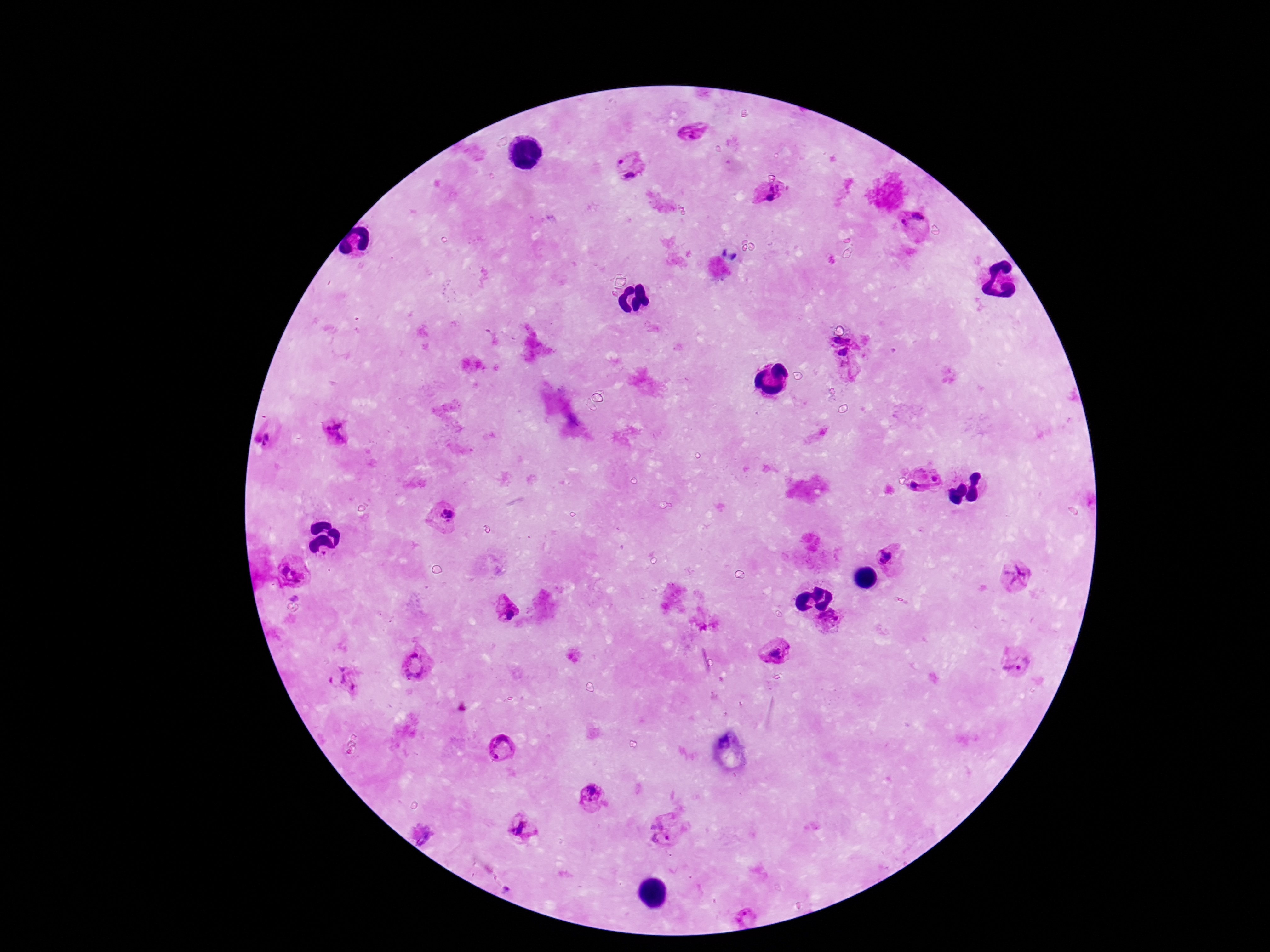 Approximate object centers, in pixels from the top-left corner. Plasmodium parasite locations: (x=693, y=132), (x=623, y=157), (x=631, y=176), (x=777, y=196), (x=912, y=223), (x=838, y=340), (x=845, y=355), (x=334, y=434), (x=268, y=440), (x=935, y=478), (x=917, y=487), (x=446, y=514), (x=888, y=556), (x=291, y=571), (x=1014, y=574), (x=506, y=607), (x=831, y=623), (x=778, y=652), (x=1016, y=660), (x=417, y=664), (x=344, y=680), (x=501, y=749), (x=592, y=796), (x=526, y=830), (x=664, y=831), (x=421, y=834). Giemsa stain. Thick blood smear. Image is 1270×952 pixels. Patient malaria status: infected. Smartphone photograph taken through the microscope eyepiece. Single field of view. 100x magnification.